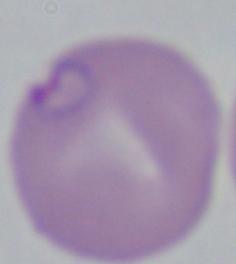

modality = photomicrograph
identification = Babesia
magnification = 1000x